Name the parasite shown.
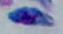

Toxoplasma gondii.

{
  "magnification": "1000x",
  "modality": "micrograph"
}